Give the extent of all Plasmodium falciparum-infected red blood cells.
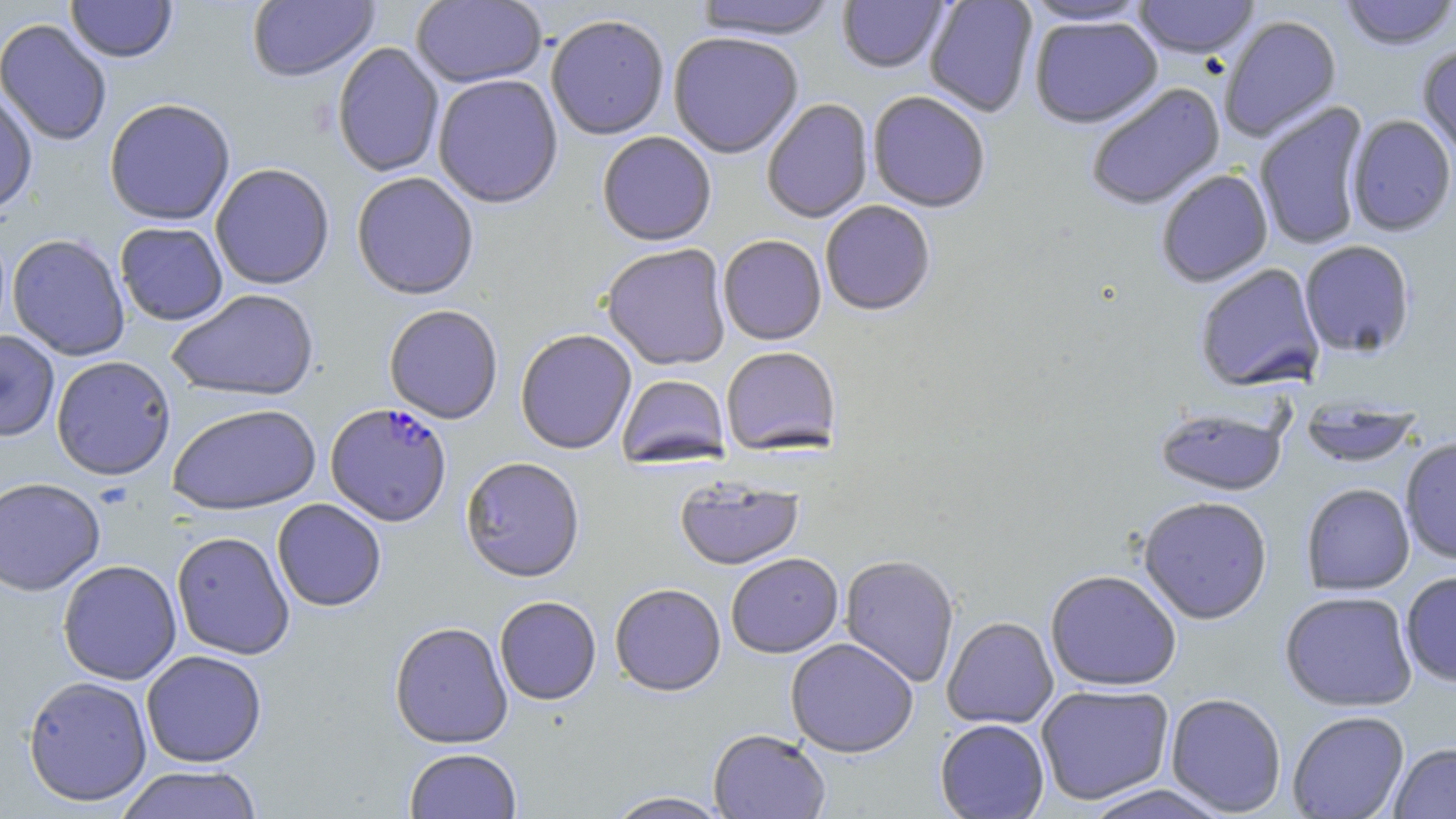

Approximate bounding boxes as [x1, y1, x2, y2] in pixels.
Plasmodium falciparum-infected red blood cells: [325, 404, 452, 528].

Summary:
  - Uninfected red blood cell locations: [66, 0, 177, 64], [247, 0, 379, 85], [411, 0, 547, 90], [693, 0, 840, 42], [837, 0, 951, 75], [924, 0, 1038, 118], [1131, 0, 1260, 60], [1338, 0, 1456, 51], [1019, 1, 1155, 27], [1219, 15, 1343, 142], [546, 16, 669, 142], [1029, 16, 1163, 130], [0, 19, 112, 147], [667, 34, 804, 161], [332, 43, 445, 179], [1416, 43, 1456, 162], [433, 76, 563, 210], [1085, 82, 1226, 211], [0, 91, 37, 220], [867, 93, 990, 214], [761, 99, 873, 224], [104, 100, 236, 227], [1254, 102, 1370, 252], [1346, 115, 1456, 237], [598, 132, 717, 248], [210, 164, 334, 291], [1156, 170, 1273, 288], [351, 174, 479, 302], [821, 201, 935, 318], [115, 223, 228, 326], [7, 234, 130, 362], [718, 237, 827, 347], [1298, 241, 1416, 359], [601, 245, 731, 372], [1194, 264, 1325, 393], [167, 290, 320, 403], [384, 306, 503, 425], [0, 330, 60, 443], [515, 330, 637, 455], [721, 348, 841, 457], [51, 357, 176, 482], [616, 375, 730, 470], [1299, 400, 1423, 469], [168, 405, 322, 517], [1154, 407, 1288, 497], [1399, 437, 1456, 564], [460, 458, 585, 584], [0, 478, 106, 596], [675, 478, 804, 572], [1301, 484, 1415, 596], [1138, 497, 1272, 625], [272, 499, 386, 612], [171, 532, 295, 660], [726, 555, 843, 659], [840, 556, 960, 688], [57, 560, 182, 685], [1045, 570, 1181, 692], [1400, 571, 1456, 688], [610, 585, 726, 698], [1279, 591, 1418, 712], [494, 596, 601, 706], [942, 618, 1058, 729], [389, 622, 513, 750], [785, 638, 918, 759], [141, 650, 267, 768], [23, 675, 153, 807], [1035, 684, 1174, 805], [1165, 694, 1287, 816], [1288, 711, 1409, 819], [935, 719, 1049, 818], [708, 731, 831, 819], [1389, 742, 1456, 819], [404, 748, 522, 819], [113, 765, 265, 818], [1078, 784, 1232, 819], [603, 791, 735, 819]
  - Slide-level diagnosis: Plasmodium falciparum
  - Modality: optical microscopy
  - Preparation: thin blood smear
  - Field of view: one of a larger specimen
  - Stain: May-Grünwald-Giemsa
  - Image size: 1456×819 pixels
  - Magnification: 1000x